Identify the blood parasite species.
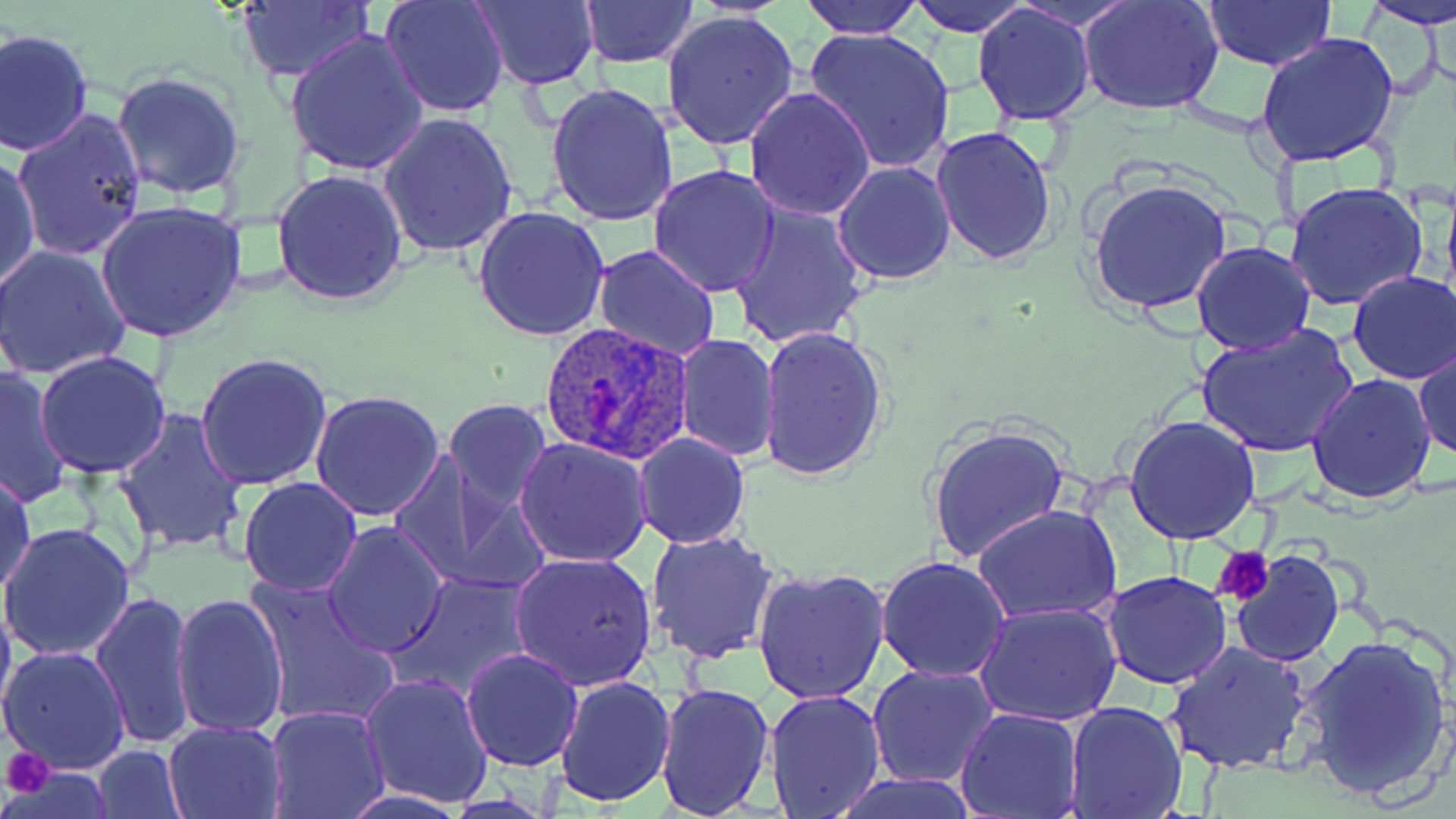

Plasmodium ovale.

Approximate bounding boxes as named x1/y1/x2/y2 corners in pixels. Uninfected red blood cell locations: (x1=379, y1=0, x2=509, y2=118), (x1=473, y1=0, x2=599, y2=90), (x1=580, y1=0, x2=697, y2=68), (x1=799, y1=0, x2=926, y2=38), (x1=903, y1=0, x2=1036, y2=37), (x1=1078, y1=0, x2=1225, y2=118), (x1=1202, y1=0, x2=1336, y2=70), (x1=1360, y1=0, x2=1456, y2=31), (x1=235, y1=3, x2=372, y2=82), (x1=972, y1=4, x2=1095, y2=127), (x1=660, y1=10, x2=798, y2=152), (x1=0, y1=27, x2=93, y2=157), (x1=803, y1=27, x2=955, y2=173), (x1=285, y1=28, x2=427, y2=176), (x1=1256, y1=31, x2=1400, y2=168), (x1=111, y1=71, x2=245, y2=201), (x1=544, y1=80, x2=679, y2=226), (x1=744, y1=85, x2=877, y2=220), (x1=12, y1=107, x2=147, y2=259), (x1=377, y1=111, x2=517, y2=257), (x1=930, y1=126, x2=1059, y2=268), (x1=1, y1=153, x2=40, y2=295), (x1=832, y1=160, x2=958, y2=284), (x1=647, y1=164, x2=781, y2=298), (x1=273, y1=169, x2=406, y2=305), (x1=1087, y1=178, x2=1232, y2=317), (x1=1285, y1=182, x2=1428, y2=311), (x1=93, y1=200, x2=247, y2=344), (x1=728, y1=201, x2=870, y2=350), (x1=472, y1=205, x2=610, y2=342), (x1=1191, y1=243, x2=1315, y2=356), (x1=1, y1=244, x2=132, y2=379), (x1=592, y1=246, x2=723, y2=364), (x1=1347, y1=272, x2=1456, y2=384), (x1=1195, y1=324, x2=1360, y2=458), (x1=757, y1=326, x2=890, y2=483), (x1=675, y1=333, x2=780, y2=462), (x1=1414, y1=343, x2=1455, y2=464), (x1=33, y1=351, x2=172, y2=480), (x1=195, y1=352, x2=331, y2=490), (x1=0, y1=366, x2=74, y2=510), (x1=1307, y1=373, x2=1436, y2=503), (x1=310, y1=389, x2=445, y2=521), (x1=442, y1=398, x2=552, y2=512), (x1=114, y1=407, x2=248, y2=555), (x1=1122, y1=414, x2=1261, y2=544), (x1=925, y1=421, x2=1068, y2=565), (x1=633, y1=433, x2=750, y2=549), (x1=514, y1=437, x2=653, y2=566), (x1=390, y1=454, x2=544, y2=597), (x1=1, y1=468, x2=37, y2=604), (x1=239, y1=476, x2=363, y2=596), (x1=972, y1=503, x2=1121, y2=623), (x1=321, y1=521, x2=448, y2=659), (x1=0, y1=523, x2=134, y2=661), (x1=644, y1=529, x2=781, y2=666), (x1=1230, y1=549, x2=1345, y2=666), (x1=510, y1=550, x2=657, y2=691), (x1=876, y1=556, x2=1010, y2=682), (x1=752, y1=566, x2=893, y2=706), (x1=1101, y1=569, x2=1232, y2=689), (x1=388, y1=572, x2=535, y2=701), (x1=246, y1=576, x2=400, y2=728), (x1=0, y1=580, x2=16, y2=731), (x1=89, y1=589, x2=196, y2=749), (x1=171, y1=594, x2=288, y2=740), (x1=973, y1=602, x2=1122, y2=728), (x1=1295, y1=631, x2=1452, y2=801), (x1=1163, y1=640, x2=1315, y2=775), (x1=0, y1=644, x2=132, y2=776), (x1=460, y1=647, x2=583, y2=772), (x1=868, y1=662, x2=1000, y2=789), (x1=360, y1=673, x2=492, y2=809), (x1=553, y1=676, x2=675, y2=807), (x1=655, y1=681, x2=776, y2=818), (x1=765, y1=687, x2=889, y2=816), (x1=1063, y1=701, x2=1188, y2=819), (x1=263, y1=706, x2=389, y2=819), (x1=955, y1=708, x2=1083, y2=819), (x1=163, y1=719, x2=288, y2=818), (x1=91, y1=745, x2=187, y2=818), (x1=7, y1=765, x2=112, y2=816), (x1=826, y1=771, x2=978, y2=819). Platelet locations: (x1=1212, y1=545, x2=1274, y2=607), (x1=2, y1=745, x2=54, y2=797). Plasmodium ovale-infected red blood cell locations: (x1=537, y1=324, x2=694, y2=464). Optical microscopy. Single field of view. Captured at 1000x magnification. May-Grünwald-Giemsa stain. Image is 1456×819 pixels. Thin blood smear.